Give the position of every malaria parasite.
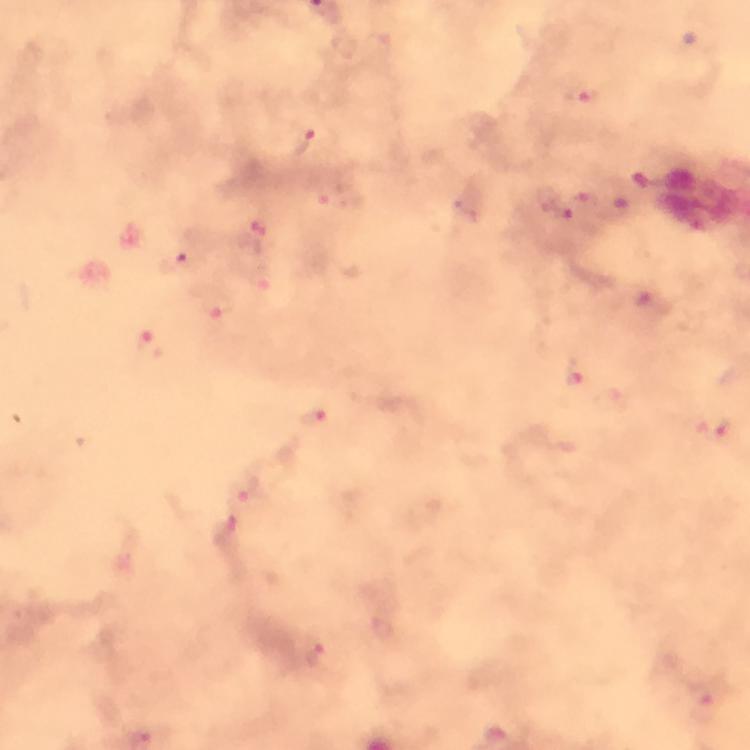

Approximate centers as {x, y} in pixels.
Malaria parasites: {584, 96}, {303, 144}, {325, 196}, {547, 197}, {263, 235}, {176, 262}, {263, 280}, {218, 305}, {150, 347}, {575, 380}, {316, 422}, {714, 428}, {247, 494}, {318, 658}.

Summary:
  - Cropped from: a single field of view
  - Preparation: thick smear
  - Context: from a malaria diagnostic workup
  - Immersion oil: used
  - Magnification: 100x
  - Stain: Giemsa
  - Capture: smartphone mounted on the microscope
  - Image size: 750×750 pixels